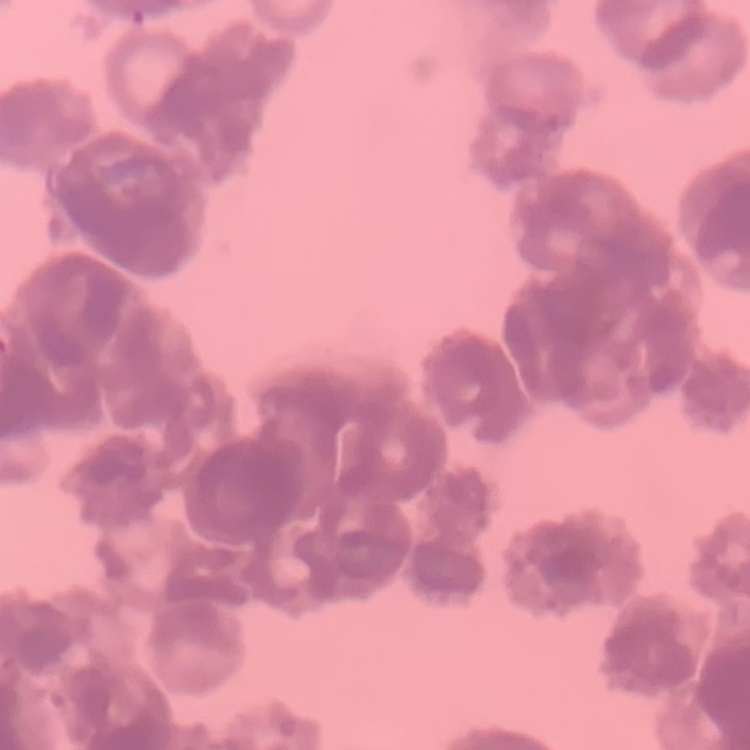
erythrocyte morphology = rouleaux formation
preparation = thin blood film
image type = square crop of a larger photomicrograph
stain = Field's or Giemsa